Assess for Plasmodium parasites.
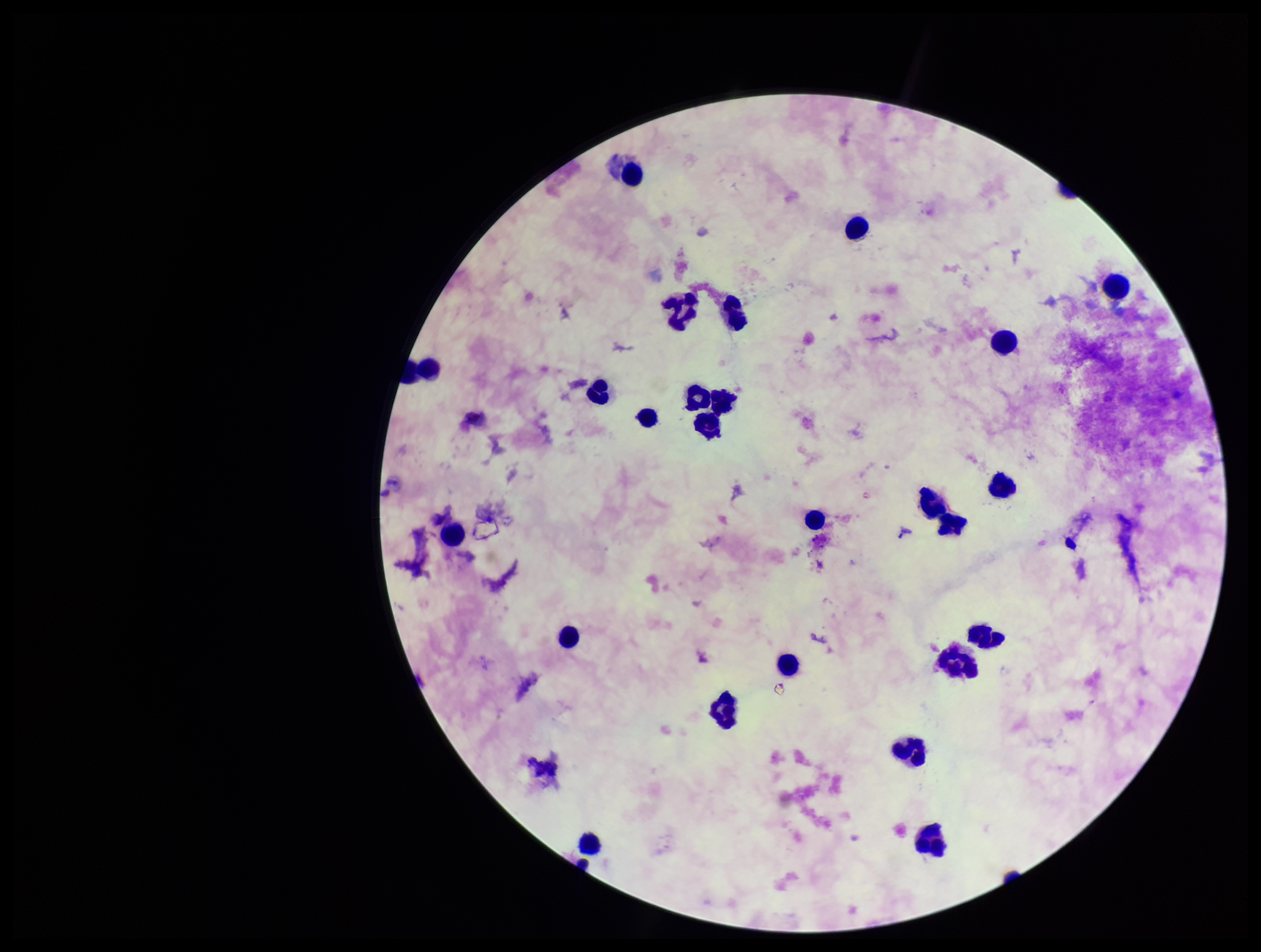
None identified.

Summary:
  - Capture: smartphone photograph through the microscope eyepiece
  - Preparation: thick blood smear
  - Patient malaria status: negative
  - Field of view: single
  - Stain: Giemsa
  - Image size: 1261×952 pixels
  - Leukocyte count: 26
  - Parasite count: 0